Locate every leukocyte (white blood cell).
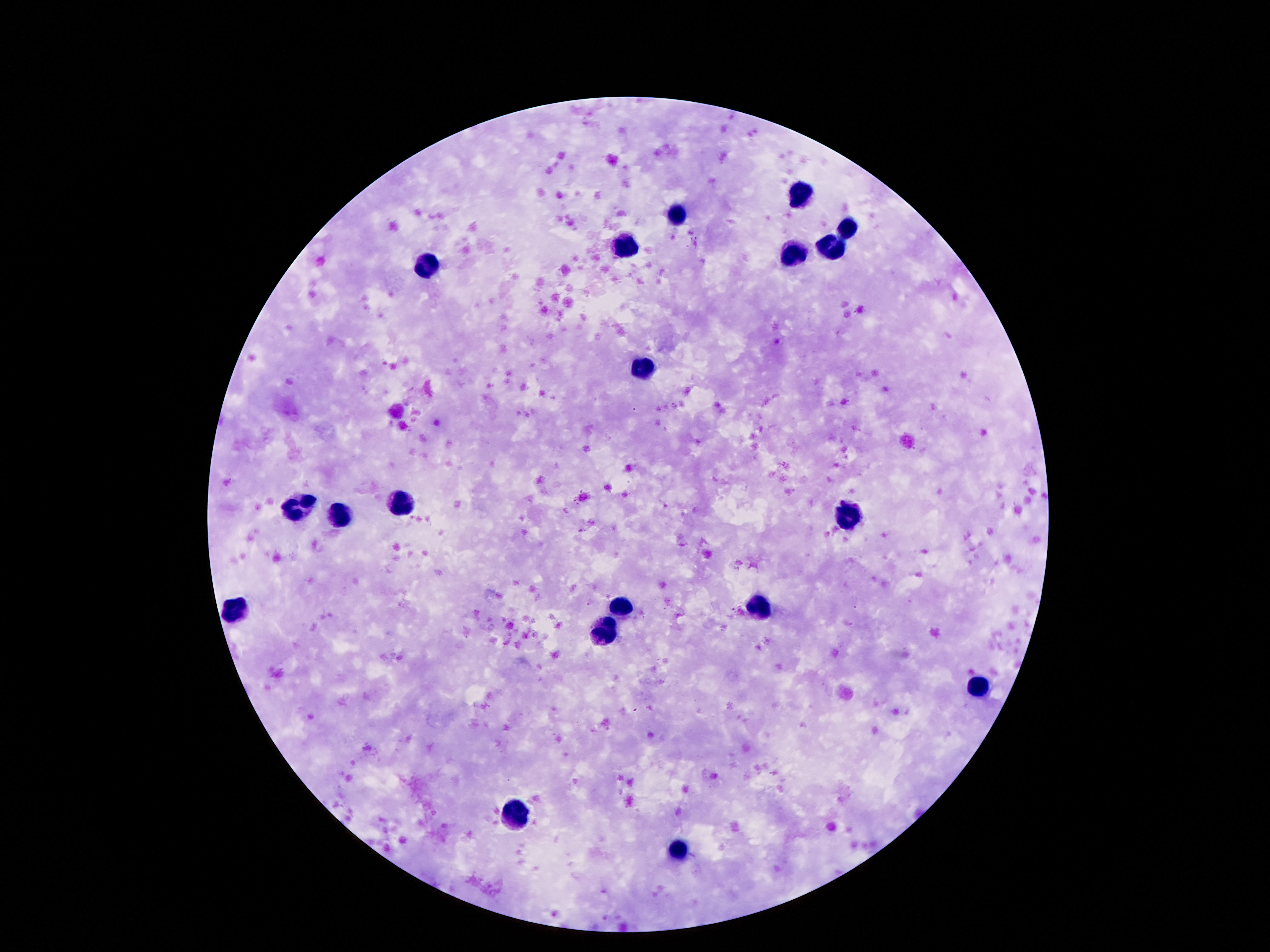
Approximate centers as (x, y) in pixels.
Leukocytes: (802, 193), (682, 213), (848, 228), (837, 244), (625, 245), (797, 252), (424, 267), (642, 367), (300, 504), (399, 507), (340, 515), (848, 518), (757, 606), (234, 608), (623, 608), (607, 633), (976, 686), (512, 814), (680, 853).

Summary:
  - Stain: Giemsa
  - Image size: 1270×952 pixels
  - Preparation: thick blood film
  - Field of view: single
  - Magnification: 100x
  - Patient malaria status: uninfected
  - Capture: smartphone camera through the microscope eyepiece